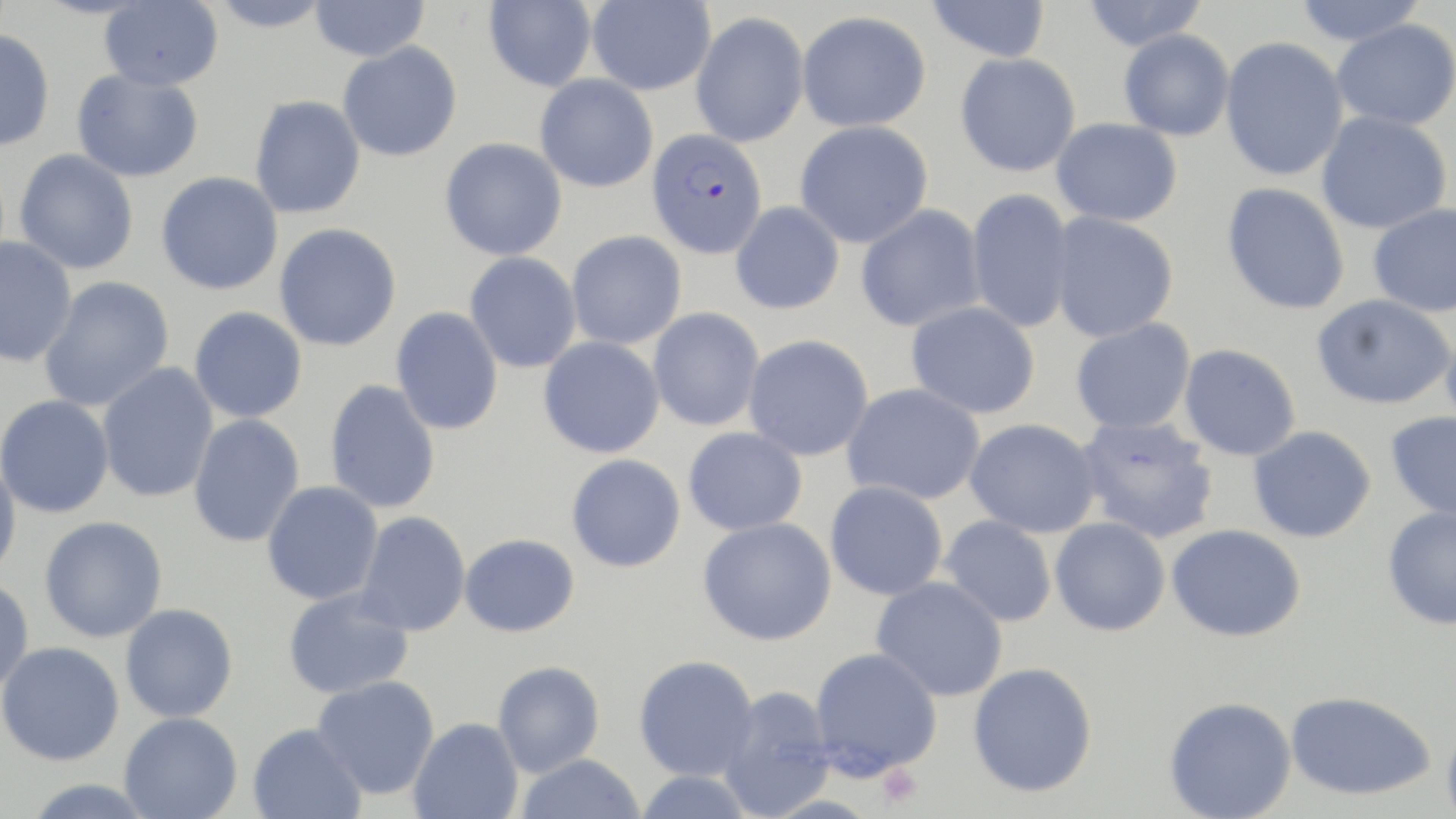

slide_level_diagnosis: Plasmodium falciparum
platelet_locations: 'approximate bounding boxes as (x1,y1)-(x2,y2) corner pairs in pixels: (877,763)-(922,809)'
magnification: 1000x
preparation: thin blood film
modality: optical microscopy
uninfected_red_blood_cell_locations: 'approximate bounding boxes as (x1,y1)-(x2,y2) corner pairs in pixels: (207,0)-(334,32), (483,0)-(597,92), (587,0)-(715,95), (925,0)-(1051,63), (1081,0)-(1210,51), (1291,0)-(1429,45), (99,1)-(223,91), (310,1)-(429,61), (796,10)-(932,132), (690,11)-(810,148), (1331,19)-(1456,130), (0,28)-(56,152), (1118,29)-(1235,141), (1220,36)-(1349,181), (337,41)-(463,162), (954,52)-(1081,177), (71,68)-(204,182), (535,73)-(658,193), (249,95)-(365,219), (1316,111)-(1452,234), (1051,117)-(1183,227), (794,120)-(933,248), (439,137)-(567,261), (14,150)-(139,274), (156,171)-(283,295), (1221,183)-(1350,315), (966,187)-(1075,334), (730,201)-(845,315), (1367,203)-(1456,317), (855,204)-(986,333), (1050,212)-(1179,343), (274,224)-(402,352), (566,230)-(687,349), (0,236)-(77,368), (464,251)-(582,373), (38,276)-(174,412), (1312,294)-(1455,410), (905,301)-(1041,419), (188,306)-(307,424), (391,306)-(504,435), (648,307)-(765,431), (1070,317)-(1196,435), (1440,323)-(1456,435), (742,334)-(874,462), (538,336)-(665,458), (1178,343)-(1301,461), (96,363)-(219,503), (324,379)-(441,514), (842,383)-(987,506), (0,394)-(115,518), (1385,411)-(1456,522), (188,414)-(305,548), (1075,415)-(1220,544), (964,418)-(1101,538), (1248,425)-(1376,543), (683,426)-(807,536), (566,454)-(686,573), (0,456)-(22,582), (825,480)-(948,601), (261,481)-(384,605), (1382,506)-(1456,630), (355,511)-(471,636), (939,515)-(1058,627), (38,516)-(168,643), (698,516)-(836,646), (1050,518)-(1170,636), (1167,523)-(1306,642), (459,533)-(580,637), (0,576)-(34,697), (871,576)-(1008,702), (282,586)-(414,700), (120,604)-(238,723), (0,641)-(124,765), (808,647)-(942,779), (633,654)-(759,781), (492,660)-(605,777), (967,662)-(1098,797), (312,675)-(439,799), (716,685)-(837,819), (1284,690)-(1436,801), (1164,696)-(1296,819), (119,712)-(243,819), (1441,716)-(1456,819), (408,717)-(523,819), (248,723)-(366,819), (515,753)-(647,819), (633,770)-(756,818), (20,778)-(158,819)'
plasmodium_falciparum_infected_red_blood_cell_locations: 'approximate bounding boxes as (x1,y1)-(x2,y2) corner pairs in pixels: (646,128)-(768,260)'
stain: May-Grünwald-Giemsa
field_of_view: single
image_size: 1456×819 pixels